Assess this cell for malaria.
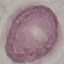
Uninfected.

Summary:
  - Capture: smartphone through the microscope eyepiece
  - Stain: Giemsa
  - Preparation: thin blood film
  - Image type: automatically extracted cell patch, resized to 64 × 64 pixels